State which cell type is depicted.
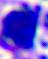
This is a leukocyte.

Summary:
  - Modality: micrograph
  - Magnification: 400x